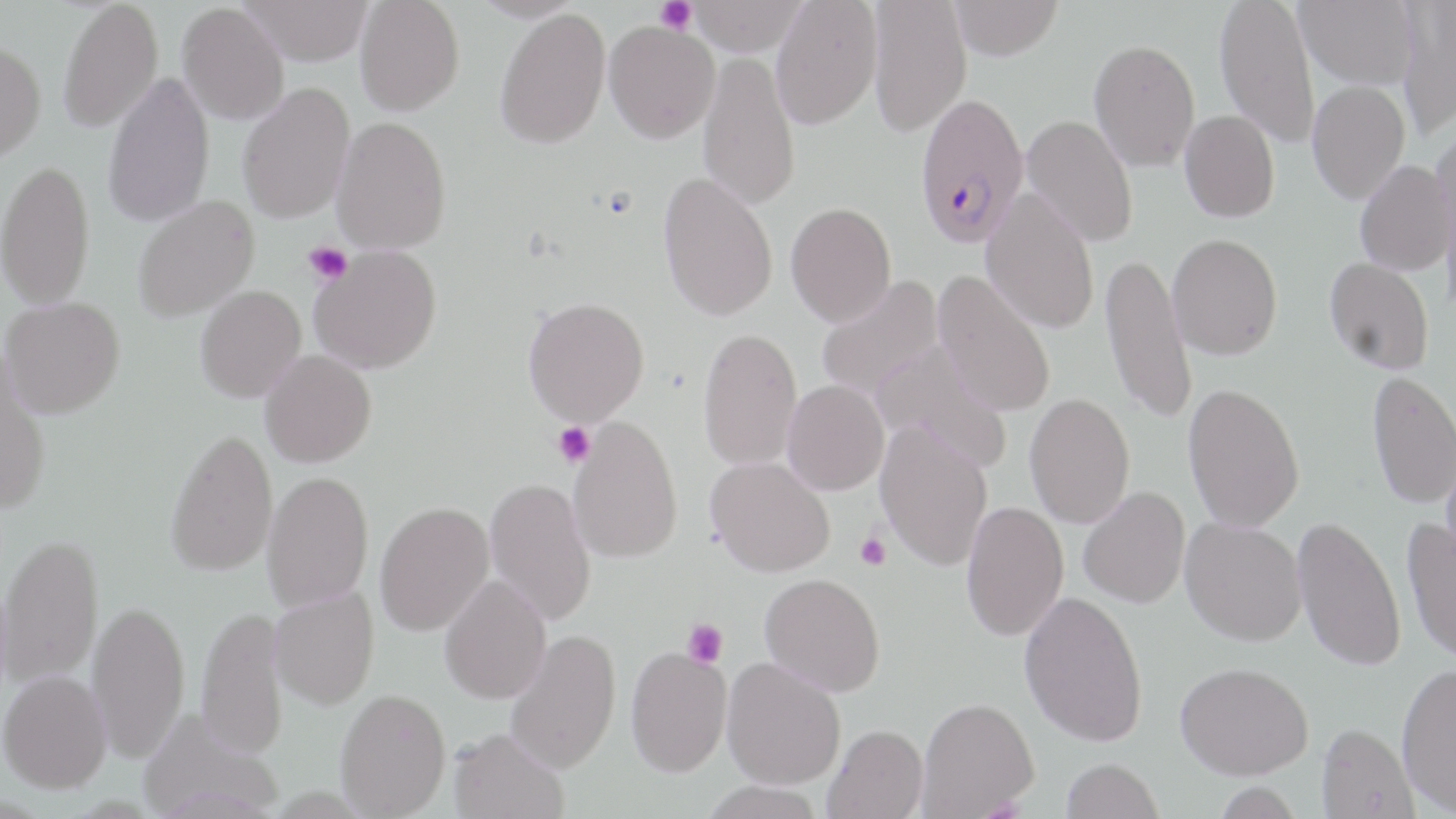
{
  "slide_level_diagnosis": "Plasmodium falciparum",
  "field_of_view": "one of a larger specimen",
  "preparation": "thin blood smear",
  "uninfected_red_blood_cell_locations": "approximate bounding boxes as (x1, y1, x2, y2) in pixels: (58, 0, 163, 133), (238, 0, 374, 65), (355, 0, 465, 116), (687, 0, 809, 55), (770, 0, 883, 129), (950, 0, 1064, 60), (1214, 0, 1320, 148), (1295, 0, 1420, 89), (868, 1, 971, 137), (1397, 1, 1456, 140), (177, 3, 289, 125), (494, 7, 611, 148), (603, 20, 720, 143), (0, 39, 46, 162), (1089, 39, 1200, 172), (698, 51, 801, 210), (103, 71, 215, 229), (1307, 79, 1410, 204), (237, 82, 355, 224), (1179, 110, 1280, 223), (1021, 114, 1138, 247), (331, 115, 452, 254), (1432, 120, 1456, 262), (0, 158, 95, 310), (1355, 160, 1454, 276), (657, 171, 778, 321), (981, 188, 1100, 334), (132, 196, 259, 322), (786, 201, 897, 326), (1167, 234, 1283, 360), (309, 245, 442, 374), (1100, 252, 1196, 426), (1324, 257, 1435, 374), (932, 270, 1057, 417), (815, 276, 944, 402), (195, 286, 306, 403), (1, 296, 126, 418), (523, 296, 650, 426), (698, 327, 803, 471), (871, 341, 1012, 471), (260, 349, 377, 467), (0, 350, 53, 516), (1367, 370, 1456, 509), (782, 379, 890, 495), (1183, 382, 1305, 533), (1025, 392, 1135, 529), (567, 417, 684, 564), (875, 421, 994, 571), (166, 427, 277, 577), (1441, 454, 1456, 575), (706, 456, 835, 578), (262, 470, 374, 612), (484, 477, 597, 627), (1078, 486, 1190, 608), (961, 500, 1069, 640), (374, 501, 495, 636), (1293, 515, 1406, 672), (1402, 516, 1456, 665), (1180, 517, 1306, 645), (0, 533, 103, 689), (760, 573, 886, 696), (440, 574, 552, 704), (270, 586, 379, 710), (1019, 591, 1149, 746), (87, 599, 190, 763), (196, 605, 288, 758), (505, 629, 621, 773), (625, 645, 733, 777), (722, 658, 846, 789), (1175, 661, 1313, 780), (1396, 662, 1456, 815), (0, 669, 111, 793), (335, 688, 451, 817), (918, 697, 1039, 817), (139, 710, 284, 818), (1317, 722, 1418, 819), (825, 724, 928, 818), (448, 726, 569, 819), (1061, 758, 1164, 818), (698, 780, 826, 819)",
  "image_size": "1456×819 pixels",
  "platelet_locations": "approximate bounding boxes as (x1, y1, x2, y2) in pixels: (656, 0, 697, 34), (304, 242, 352, 284), (553, 422, 595, 468), (855, 532, 891, 570), (682, 618, 728, 668)",
  "modality": "optical microscopy",
  "magnification": "1000x",
  "stain": "May-Grünwald-Giemsa",
  "plasmodium_falciparum_infected_red_blood_cell_locations": "approximate bounding boxes as (x1, y1, x2, y2) in pixels: (912, 91, 1030, 249)"
}